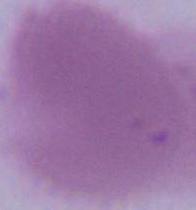
An erythrocyte is seen. Captured at 1000x magnification. Micrograph.